Locate every uninfected red blood cell.
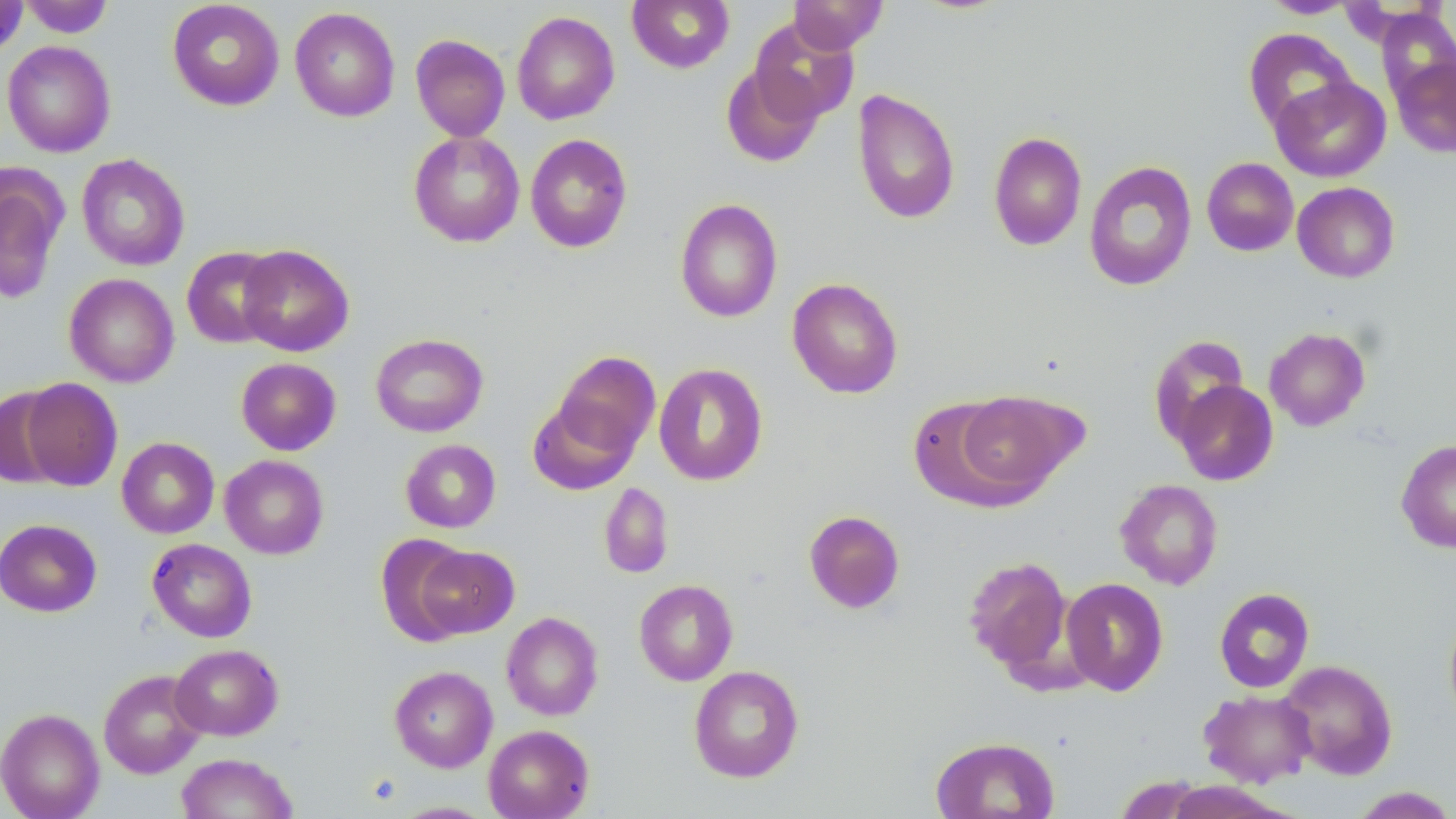
Approximate bounding boxes as (x1,y1)-(x2,y2) corner pairs in pixels.
Uninfected red blood cells: (20,0)-(113,38), (167,0)-(284,111), (627,0)-(734,73), (0,1)-(28,58), (788,1)-(888,54), (1260,1)-(1360,19), (289,6)-(400,122), (1375,8)-(1456,107), (511,11)-(620,125), (749,18)-(858,124), (1242,28)-(1357,133), (410,34)-(510,141), (2,40)-(116,157), (1390,54)-(1456,159), (721,62)-(826,167), (1271,76)-(1390,182), (852,89)-(960,225), (408,130)-(525,247), (988,132)-(1087,251), (525,134)-(633,253), (77,153)-(190,271), (1202,157)-(1299,256), (1083,160)-(1197,292), (0,168)-(67,305), (1292,182)-(1400,282), (674,198)-(783,323), (237,244)-(354,356), (181,246)-(284,348), (64,273)-(179,387), (787,277)-(904,398), (1264,327)-(1371,431), (370,333)-(488,437), (1148,335)-(1250,447), (551,350)-(660,459), (236,358)-(341,455), (653,363)-(768,487), (20,378)-(123,491), (1174,380)-(1278,486), (0,388)-(69,488), (951,390)-(1083,499), (528,395)-(641,495), (906,396)-(1028,510), (116,436)-(219,538), (400,439)-(501,533), (1396,439)-(1456,553), (219,454)-(329,559), (1115,479)-(1223,590), (599,482)-(674,579), (803,510)-(905,613), (0,518)-(102,616), (375,534)-(474,645), (147,538)-(257,642), (415,544)-(520,639), (963,555)-(1072,674), (1061,577)-(1169,696), (634,579)-(738,686), (1214,587)-(1315,693), (1444,608)-(1456,727), (501,612)-(603,721), (170,644)-(283,740), (1277,660)-(1398,779), (389,665)-(498,772), (688,665)-(804,783), (98,669)-(207,778), (1199,690)-(1316,787), (0,707)-(104,819), (483,724)-(595,819), (929,736)-(1060,818), (175,752)-(298,818), (1347,786)-(1456,818), (389,800)-(497,818).

Summary:
  - Slide-level diagnosis: no evidence of blood parasites
  - Magnification: 1000x
  - Image size: 1456×819 pixels
  - Stain: May-Grünwald-Giemsa
  - Modality: optical microscopy
  - Preparation: thin blood film
  - Field of view: one of a larger specimen